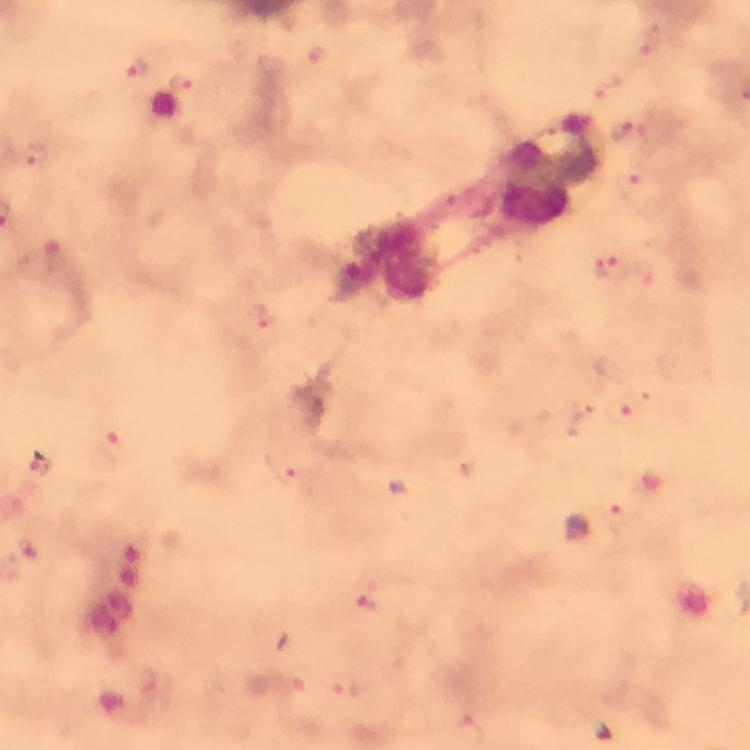

Plasmodium parasite locations = approximate object centers, in pixels from the top-left corner: (x=651, y=42), (x=317, y=56), (x=136, y=69), (x=182, y=83), (x=605, y=88), (x=634, y=135), (x=37, y=157), (x=609, y=268), (x=265, y=319), (x=634, y=407), (x=115, y=447), (x=41, y=466), (x=289, y=470), (x=614, y=518), (x=366, y=604), (x=297, y=682), (x=348, y=686)
cropped from = one field of view
image size = 750×750 pixels
magnification = 100x
context = from a diagnostic examination for malaria
capture = smartphone mounted on the microscope
stain = Giemsa
preparation = thick blood smear
immersion oil = used
leukocyte locations = approximate object centers, in pixels from the top-left corner: (x=549, y=170), (x=388, y=264)